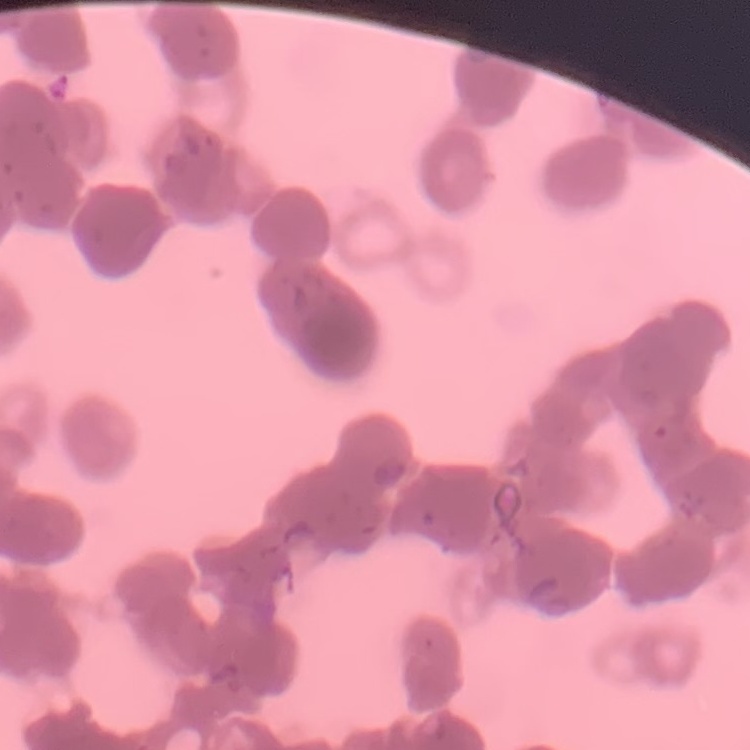 The red blood cells exhibit rouleaux formation. Square crop of a larger photomicrograph. Stained with either Field's or Giemsa. Thin peripheral smear.